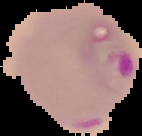
Summary:
  - Image size: 142×136 pixels
  - Image type: cell region segmented out of the field of view; surrounding area masked to black
  - Preparation: thin blood smear
  - Malaria status: parasitized